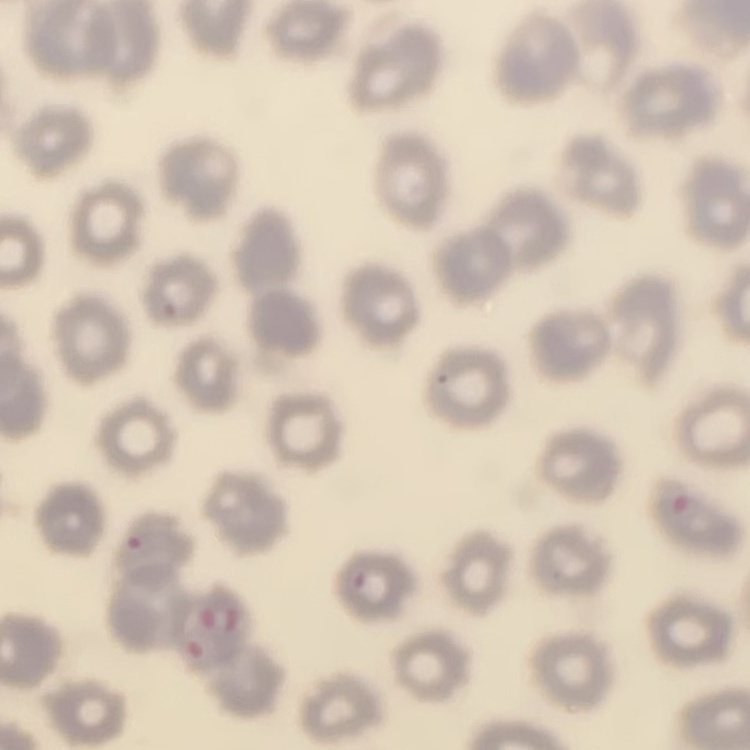

The erythrocytes show no rouleaux formation. Thin blood film. Stained with either Field's or Giemsa. Square crop of a larger photomicrograph.